Locate every Plasmodium parasite.
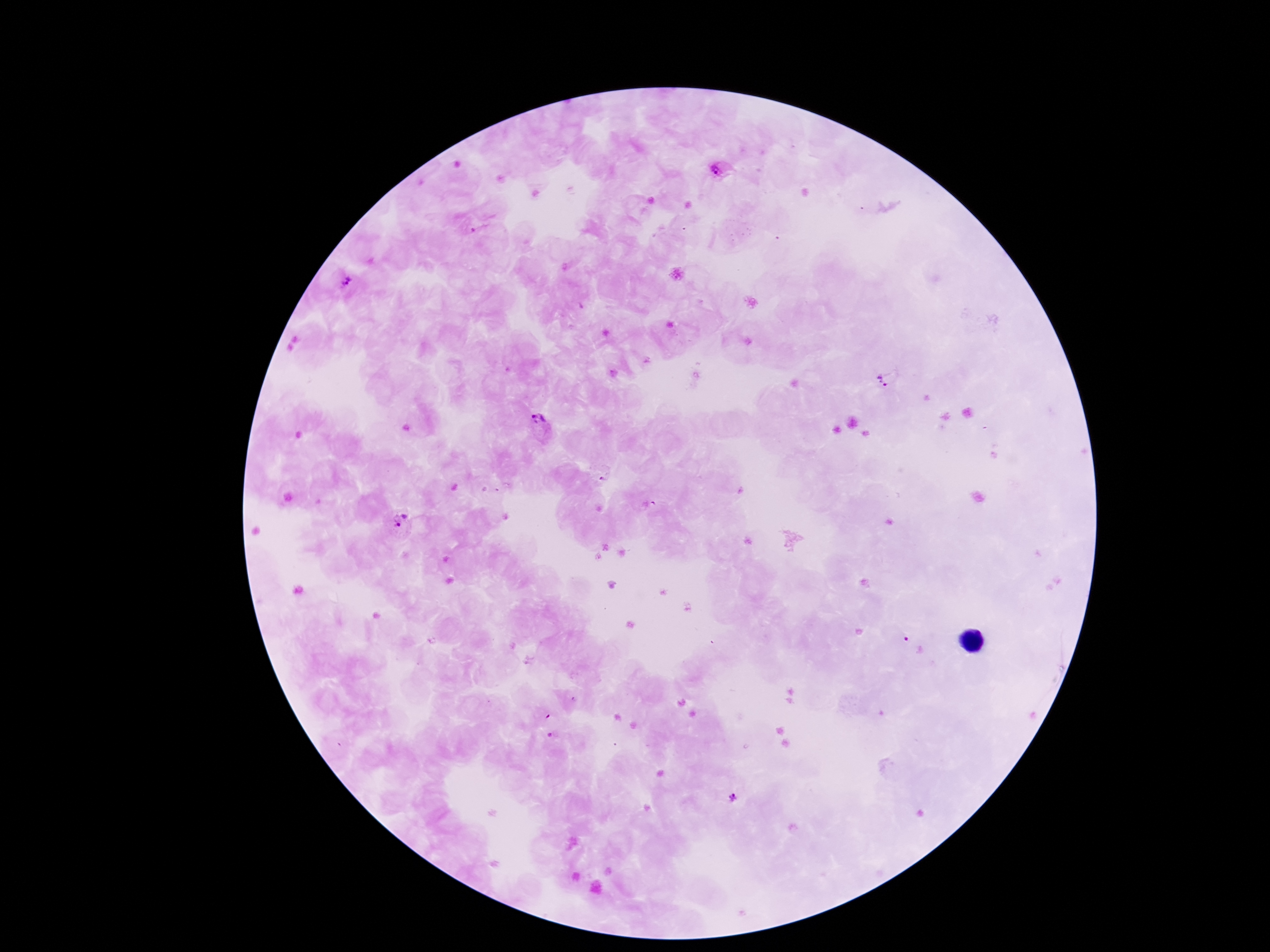
Approximate object centers, in pixels from the top-left corner.
Plasmodium parasites: (x=721, y=169), (x=346, y=280), (x=889, y=379), (x=538, y=420), (x=649, y=507), (x=401, y=520), (x=734, y=798).

Summary:
  - Field of view: single
  - Stain: Giemsa
  - Patient malaria status: positive
  - Capture: smartphone camera through the microscope eyepiece
  - Magnification: 100x
  - Preparation: thick blood smear
  - Image size: 1270×952 pixels